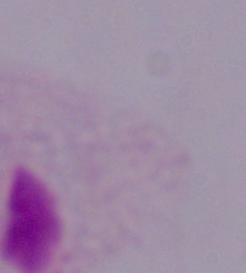
A trichomonad is shown. Photomicrograph. 1000x magnification.